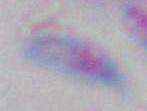

Summary:
  - Modality: micrograph
  - Identification: Toxoplasma gondii
  - Magnification: 1000x